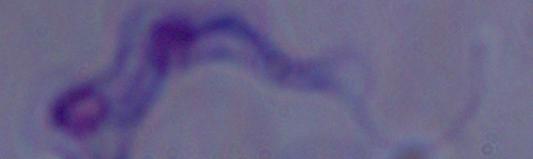
A trypanosome is seen. Micrograph. 1000x magnification.